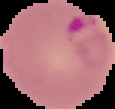

Malaria status: parasitized. Image is 115×109 pixels. Segmented cell region on a black background. From a thin blood film.